Comment on the morphology of the erythrocytes.
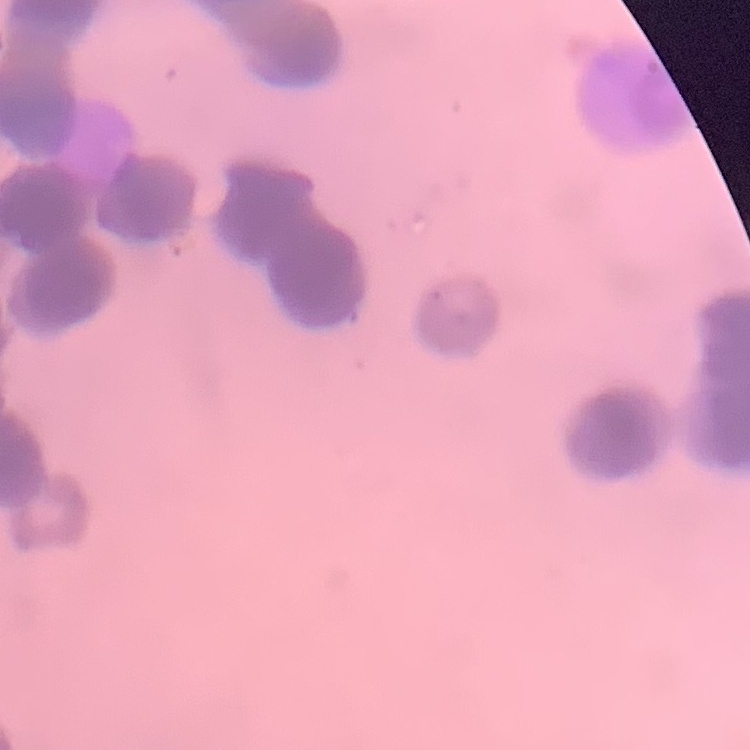

Rouleaux formation.

{
  "stain": "Field's or Giemsa",
  "preparation": "thin peripheral smear",
  "image_type": "square crop of a larger photomicrograph"
}